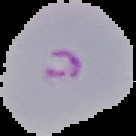

image_type: segmented cell region with the area outside set to black
image_size: 136×136 pixels
preparation: thin blood film
malaria_status: parasitized